Assess this cell for malaria.
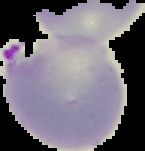
Parasitized.

Summary:
  - Preparation: thin blood smear
  - Image type: segmented cell region on a black background
  - Image size: 145×151 pixels